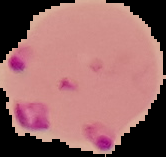

image size = 166×157 pixels
preparation = thin blood film
result = malaria parasites identified
image type = cell region segmented out of the field of view; surrounding area masked to black